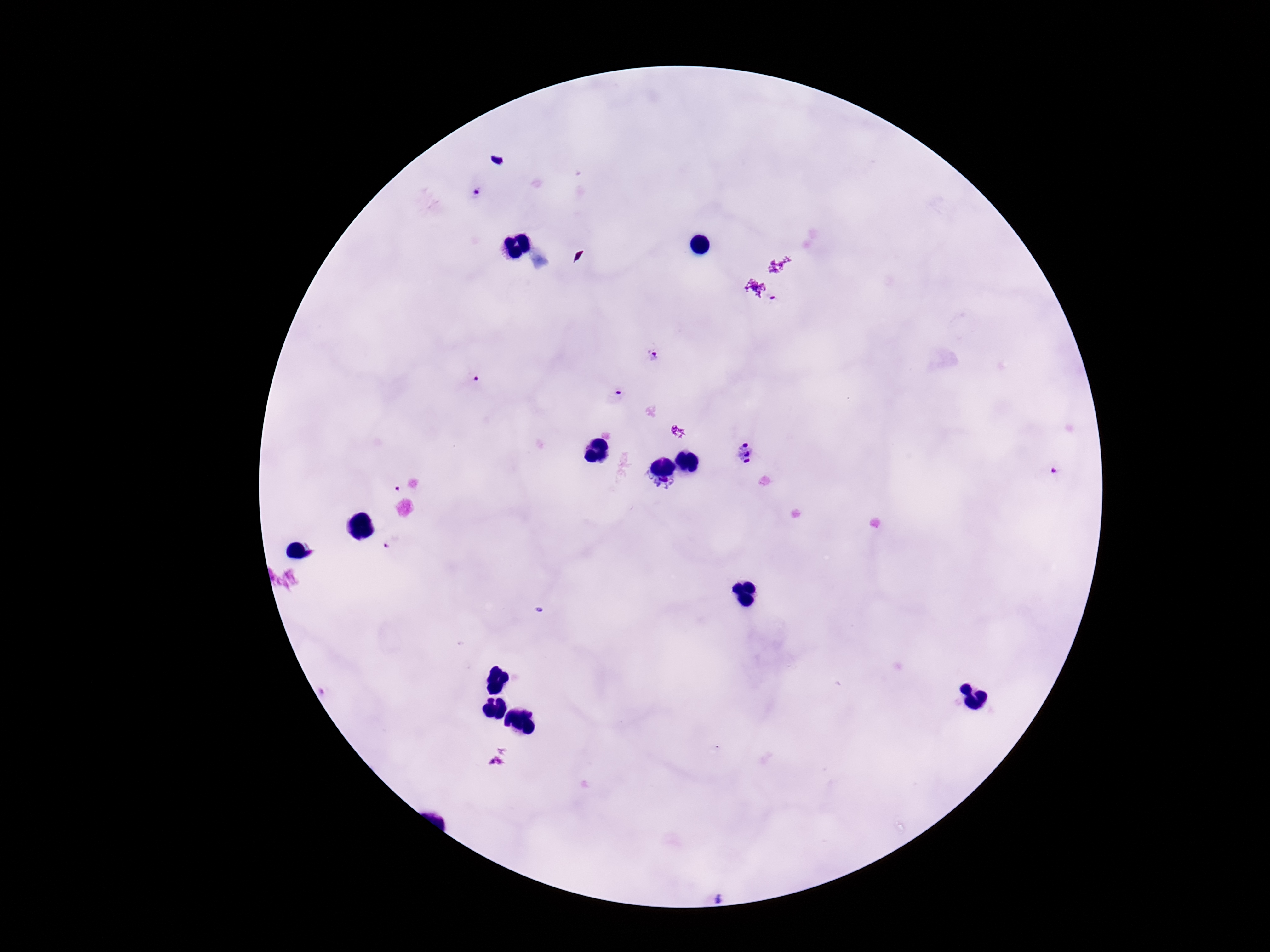

field of view = single
image size = 1270×952 pixels
patient malaria status = positive
preparation = thick blood smear
capture = smartphone camera through the microscope eyepiece
stain = Giemsa
Plasmodium parasite locations = approximate centers as {x, y} in pixels: {478, 192}, {655, 354}, {474, 383}, {615, 394}, {745, 453}, {1053, 470}, {394, 488}, {388, 542}, {719, 899}
magnification = 100x